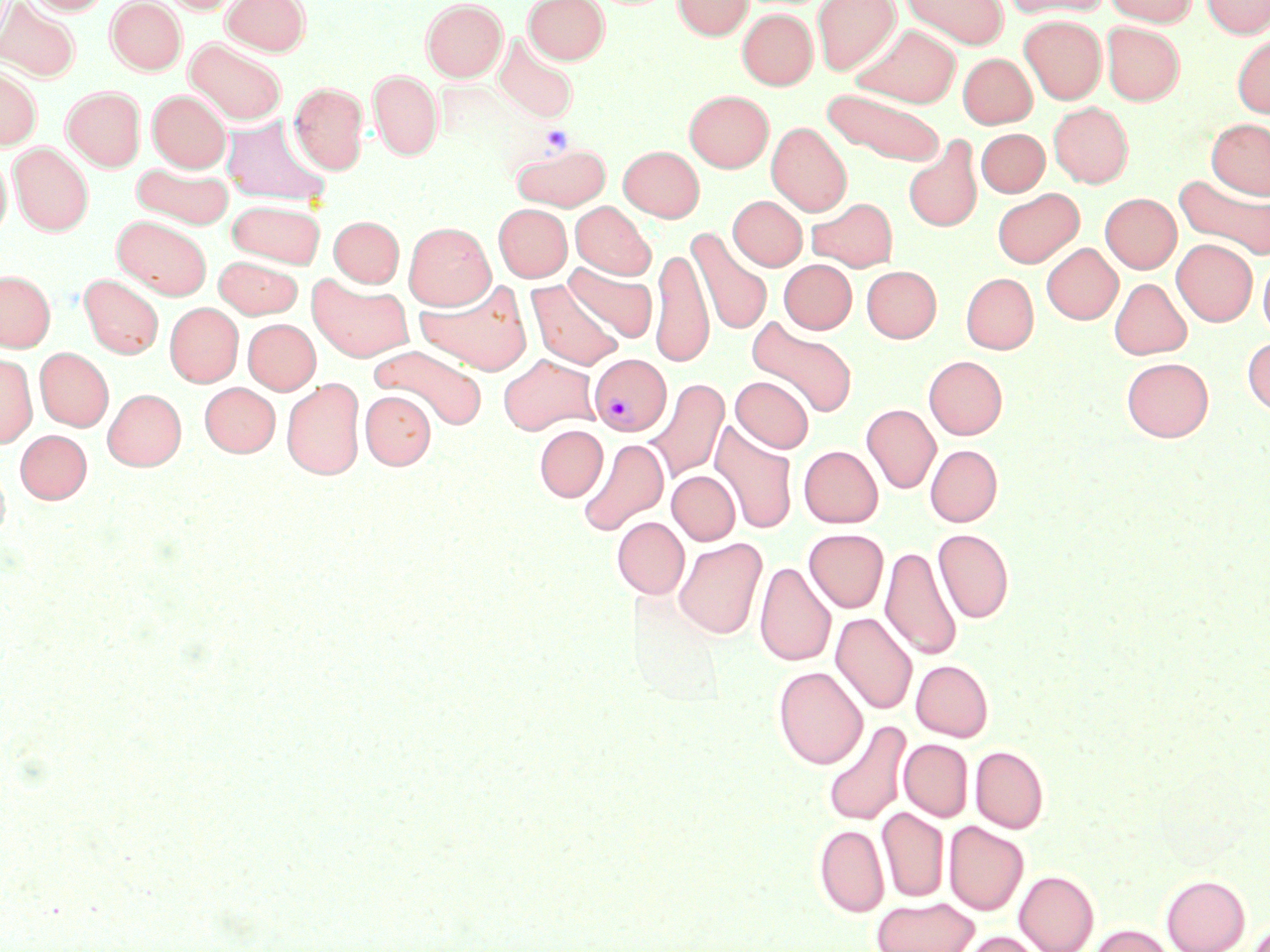 Approximate bounding boxes as (x1,y1)-(x2,y2) corner pairs in pixels. Plasmodium vivax-infected red blood cell locations: (589,354)-(671,436). Uninfected red blood cell locations: (27,0)-(110,15), (107,0)-(186,74), (162,0)-(243,14), (222,0)-(310,55), (422,0)-(507,81), (524,0)-(609,64), (672,0)-(753,39), (811,0)-(900,75), (901,0)-(1008,48), (1001,0)-(1110,19), (1104,0)-(1198,26), (1202,0)-(1270,38), (0,1)-(80,81), (738,9)-(817,90), (1020,15)-(1106,104), (1101,22)-(1184,105), (853,23)-(960,108), (1232,33)-(1270,117), (493,34)-(578,124), (185,38)-(287,125), (957,53)-(1036,128), (0,67)-(41,149), (369,70)-(443,159), (290,82)-(368,173), (62,86)-(146,171), (822,88)-(946,166), (148,90)-(230,172), (684,90)-(773,172), (1049,102)-(1133,187), (221,115)-(330,206), (1206,118)-(1270,199), (767,122)-(851,216), (976,128)-(1049,197), (903,137)-(983,232), (10,143)-(93,235), (511,143)-(610,210), (618,145)-(704,221), (0,157)-(11,239), (132,162)-(234,229), (1175,174)-(1270,261), (992,188)-(1084,268), (1100,193)-(1181,273), (728,196)-(807,270), (807,197)-(897,271), (227,200)-(326,267), (570,201)-(655,279), (493,203)-(572,282), (113,215)-(211,299), (329,216)-(403,287), (404,222)-(495,310), (687,228)-(772,335), (1172,238)-(1257,326), (1041,243)-(1122,324), (650,247)-(714,367), (1258,255)-(1270,340), (214,256)-(303,318), (780,259)-(856,333), (564,264)-(657,342), (861,265)-(941,342), (0,270)-(55,351), (961,273)-(1038,353), (79,274)-(163,359), (308,275)-(413,362), (1118,277)-(1199,442), (1110,278)-(1192,359), (415,279)-(533,375), (527,279)-(624,370), (165,302)-(243,387), (747,317)-(857,419), (243,319)-(320,394), (1243,336)-(1270,417), (372,345)-(486,431), (35,347)-(113,431), (0,353)-(37,448), (499,354)-(600,435), (924,355)-(1007,439), (1122,357)-(1213,441), (731,376)-(814,453), (282,378)-(365,480), (645,378)-(730,483), (200,383)-(280,456), (103,388)-(186,470), (360,390)-(435,469), (861,404)-(941,494), (710,421)-(798,534), (534,425)-(607,502), (15,429)-(92,503), (578,438)-(668,536), (925,444)-(1002,526), (799,445)-(883,527), (0,459)-(10,544), (667,470)-(740,545), (612,516)-(689,599), (804,528)-(888,612), (933,528)-(1013,623), (674,537)-(767,639), (880,545)-(963,661), (755,561)-(836,667), (831,612)-(917,715), (911,659)-(993,741), (773,666)-(868,769), (822,720)-(911,826), (899,739)-(972,821), (971,745)-(1049,833), (877,807)-(949,902), (945,821)-(1028,915), (814,824)-(889,916), (1015,870)-(1099,952), (1161,874)-(1250,952), (871,896)-(979,952), (1089,924)-(1175,952), (960,931)-(1046,952). Slide-level diagnosis: Plasmodium vivax. May-Grünwald-Giemsa-stained preparation. 1000x magnification. Optical microscopy. One field of a larger specimen. Image is 1270×952 pixels. Thin blood film.